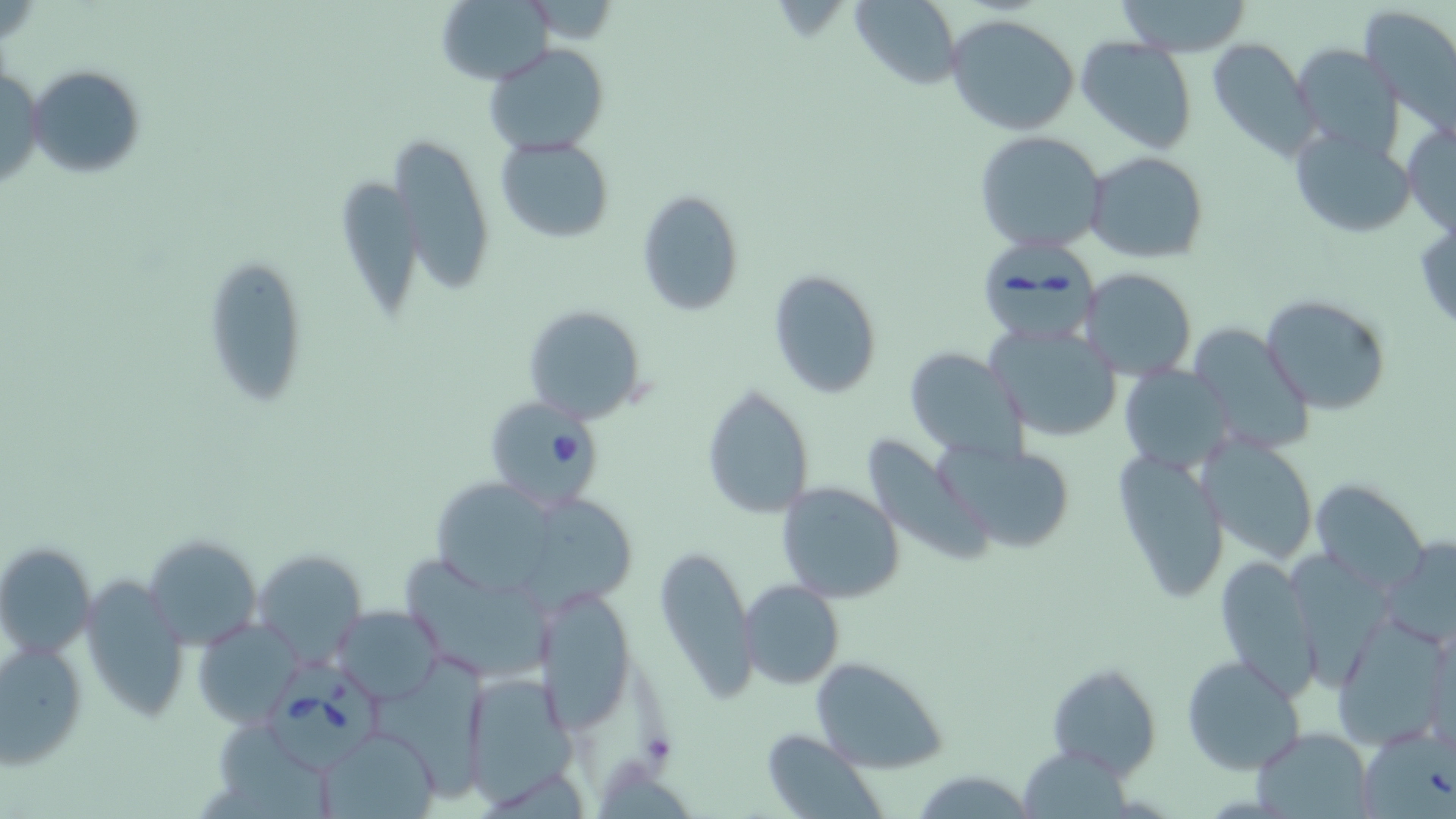

Approximate bounding boxes as named x1/y1/x2/y2 corners in pixels. Uninfected red blood cell locations: (x1=847, y1=0, x2=963, y2=90), (x1=1115, y1=0, x2=1256, y2=56), (x1=434, y1=1, x2=549, y2=82), (x1=1359, y1=5, x2=1456, y2=129), (x1=944, y1=13, x2=1081, y2=136), (x1=1076, y1=36, x2=1199, y2=154), (x1=1207, y1=38, x2=1322, y2=163), (x1=484, y1=42, x2=609, y2=156), (x1=1291, y1=42, x2=1408, y2=158), (x1=27, y1=64, x2=147, y2=180), (x1=0, y1=67, x2=44, y2=192), (x1=1402, y1=120, x2=1456, y2=237), (x1=1289, y1=127, x2=1417, y2=237), (x1=974, y1=130, x2=1108, y2=254), (x1=392, y1=135, x2=495, y2=300), (x1=496, y1=136, x2=615, y2=241), (x1=1085, y1=150, x2=1209, y2=265), (x1=336, y1=173, x2=424, y2=315), (x1=636, y1=189, x2=744, y2=317), (x1=1413, y1=217, x2=1456, y2=337), (x1=200, y1=254, x2=312, y2=410), (x1=1078, y1=267, x2=1197, y2=378), (x1=767, y1=269, x2=884, y2=399), (x1=1262, y1=294, x2=1391, y2=415), (x1=522, y1=304, x2=649, y2=426), (x1=1186, y1=322, x2=1315, y2=455), (x1=985, y1=326, x2=1124, y2=444), (x1=903, y1=346, x2=1028, y2=462), (x1=1121, y1=368, x2=1234, y2=473), (x1=702, y1=385, x2=815, y2=520), (x1=859, y1=431, x2=998, y2=567), (x1=931, y1=435, x2=1076, y2=551), (x1=1201, y1=435, x2=1318, y2=566), (x1=1115, y1=451, x2=1228, y2=603), (x1=1312, y1=480, x2=1428, y2=591), (x1=775, y1=481, x2=906, y2=604), (x1=436, y1=482, x2=556, y2=594), (x1=523, y1=498, x2=646, y2=618), (x1=143, y1=533, x2=262, y2=650), (x1=1382, y1=539, x2=1456, y2=644), (x1=654, y1=541, x2=755, y2=702), (x1=0, y1=542, x2=95, y2=662), (x1=253, y1=549, x2=368, y2=662), (x1=400, y1=553, x2=562, y2=678), (x1=1212, y1=553, x2=1320, y2=697), (x1=1291, y1=554, x2=1395, y2=686), (x1=77, y1=575, x2=190, y2=726), (x1=740, y1=579, x2=845, y2=690), (x1=534, y1=586, x2=637, y2=736), (x1=333, y1=605, x2=443, y2=702), (x1=1332, y1=619, x2=1450, y2=748), (x1=192, y1=620, x2=300, y2=727), (x1=1, y1=641, x2=87, y2=769), (x1=807, y1=655, x2=946, y2=774), (x1=1180, y1=655, x2=1306, y2=775), (x1=373, y1=657, x2=501, y2=806), (x1=1046, y1=662, x2=1161, y2=778), (x1=462, y1=669, x2=576, y2=804), (x1=224, y1=726, x2=324, y2=819), (x1=1252, y1=726, x2=1373, y2=818), (x1=316, y1=727, x2=442, y2=818), (x1=1355, y1=727, x2=1456, y2=819), (x1=759, y1=729, x2=882, y2=817), (x1=1020, y1=745, x2=1137, y2=819), (x1=910, y1=769, x2=1032, y2=817). Babesia divergens-infected red blood cell locations: (x1=979, y1=229, x2=1105, y2=346), (x1=484, y1=403, x2=601, y2=505), (x1=261, y1=660, x2=386, y2=777). Slide-level diagnosis: Babesia divergens. Thin blood film. Single field of view. Captured at 1000x magnification. Image is 1456×819 pixels. May-Grünwald-Giemsa-stained preparation. Optical microscopy.